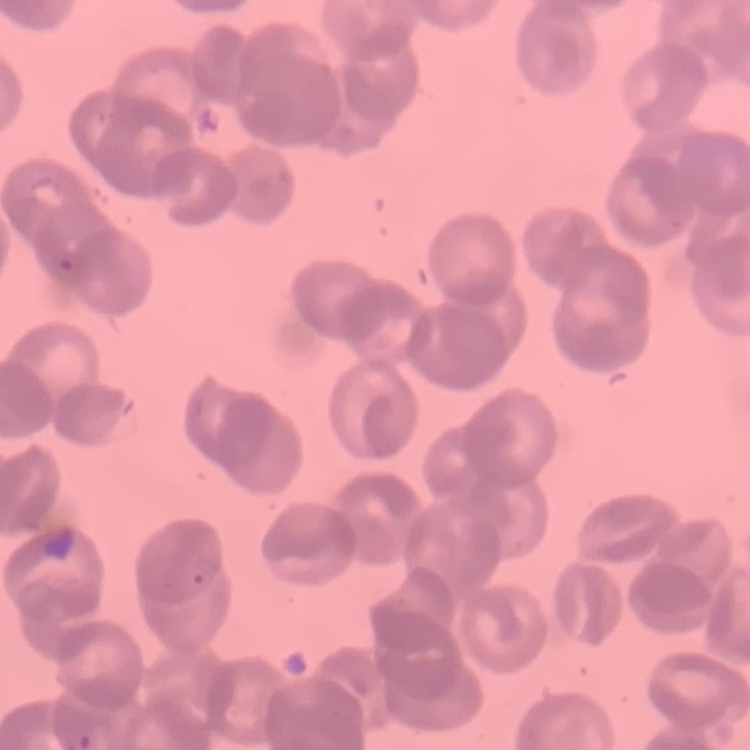
Summary:
  - Red blood cell morphology: rouleaux formation
  - Image type: square crop of a larger photomicrograph
  - Stain: Field's or Giemsa
  - Preparation: thin blood film